Name the parasite shown.
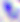
Toxoplasma gondii.

Summary:
  - Modality: photomicrograph
  - Magnification: 400x